Describe the morphology of the red blood cells.
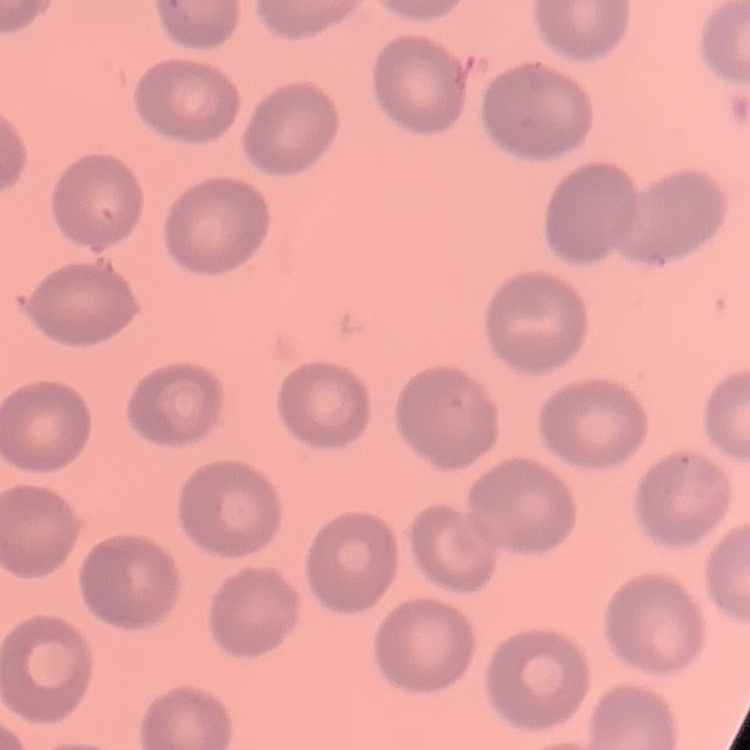

No rouleaux formation.

{
  "image_type": "one tile cut from a larger photomicrograph",
  "preparation": "thin peripheral smear",
  "stain": "Field's or Giemsa"
}